Name the parasite shown.
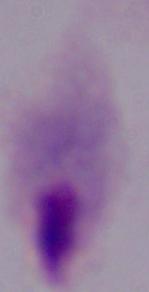

This is a trichomonad.

Summary:
  - Modality: photomicrograph
  - Magnification: 1000x